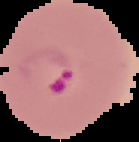
malaria status = parasitized
image size = 139×142 pixels
image type = segmented cell region with the area outside set to black
preparation = thin blood film